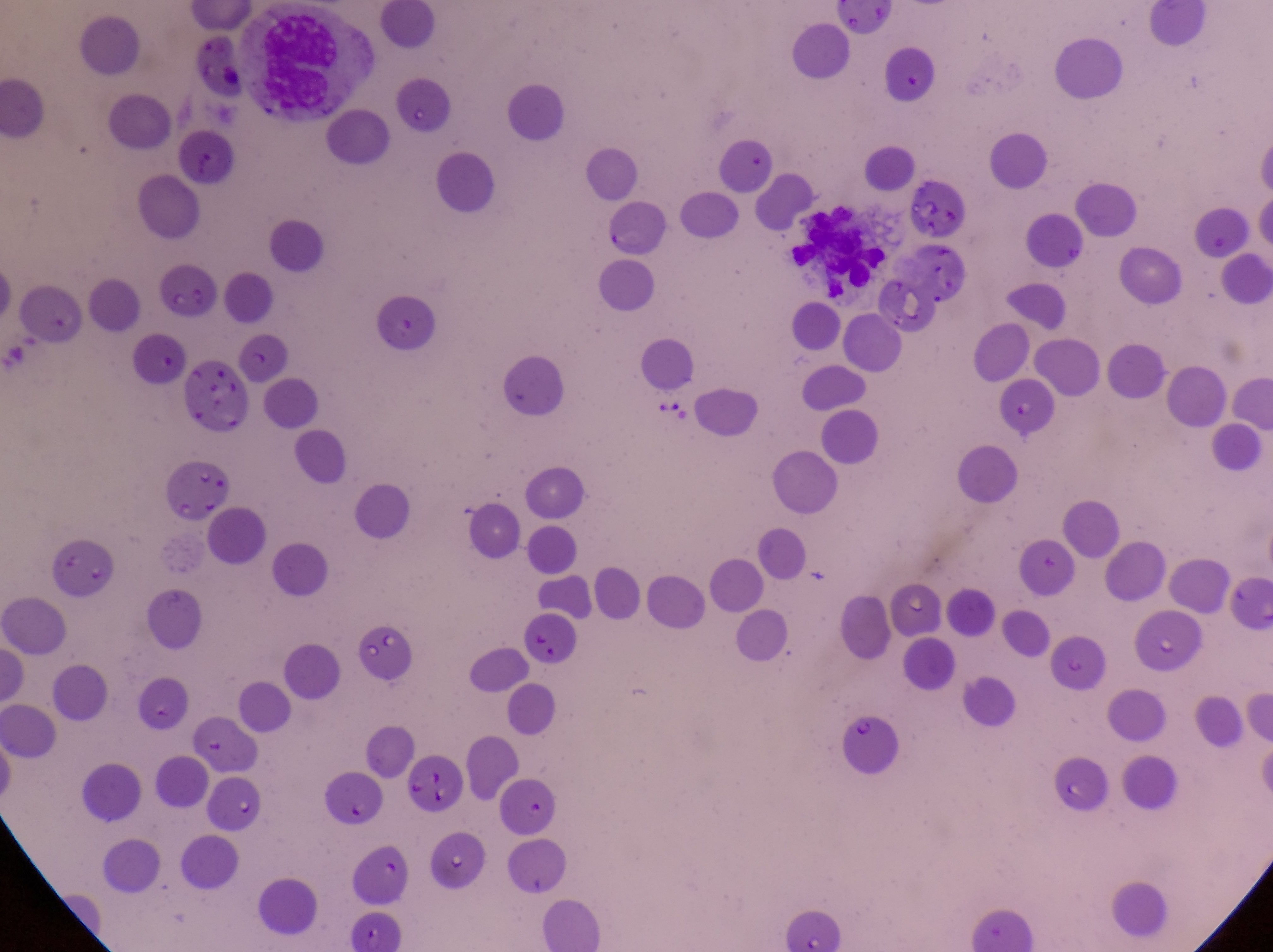

country = Uganda
magnification = 1000x
field of view = single
image size = 1273×952 pixels
artifact (platelet-like body, stain precipitate, or debris) locations = approximate bounding boxes as (left, top, right, bottom) in pixels: (906, 165, 966, 239), (183, 359, 246, 437), (651, 382, 690, 432), (357, 627, 426, 690)
preparation = thin blood film
capture = smartphone photograph through the eyepiece of an Olympus CX-23 microscope
leukocyte locations = approximate bounding boxes as (left, top, right, bottom) in pixels: (256, 10, 339, 110), (786, 199, 888, 296)